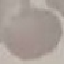
Summary:
  - Malaria status: uninfected
  - Stain: Giemsa
  - Image type: cell patch, automatically extracted from a larger field of view and resized to 64 × 64 pixels
  - Capture: smartphone through the microscope eyepiece
  - Preparation: thin smear